Classify this cell by malaria status.
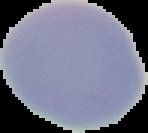
It is uninfected.

image_size: 148×133 pixels
preparation: thin blood smear
image_type: segmented cell region on a black background